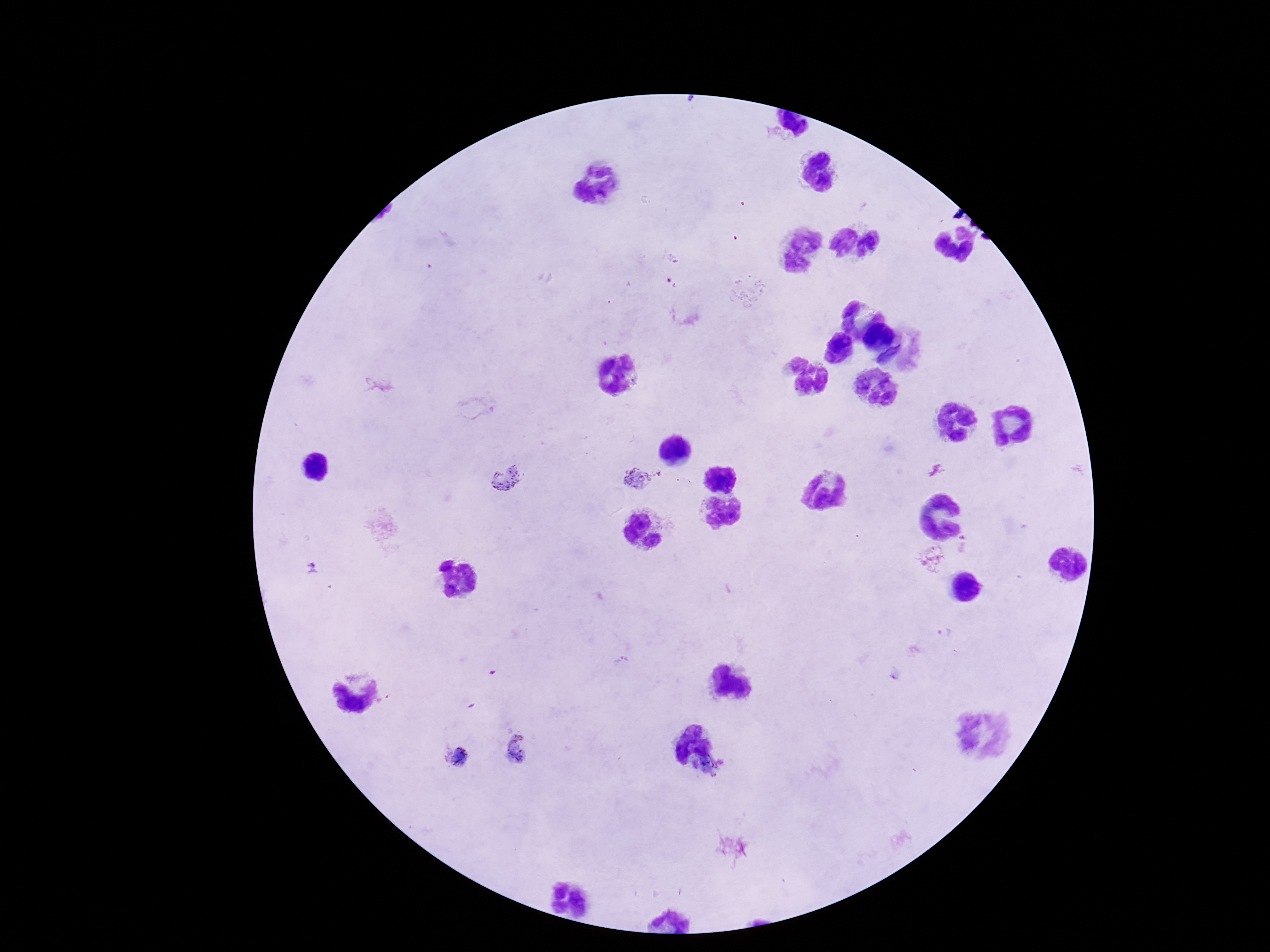
Approximate centers as {x, y} in pixels.
Summary:
  - Plasmodium parasite locations: {638, 478}, {504, 479}, {964, 543}, {932, 555}, {312, 568}, {518, 748}, {455, 758}
  - Capture: smartphone camera through the microscope eyepiece
  - Preparation: thick blood smear
  - Stain: Giemsa
  - Magnification: 100x
  - Field of view: one from this slide
  - Image size: 1270×952 pixels
  - Patient malaria status: positive